Report the malaria status of this cell.
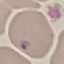
Uninfected.

Summary:
  - Preparation: thin blood film
  - Capture: smartphone through the microscope eyepiece
  - Image type: cell patch, automatically extracted from a larger field of view and resized to 64 × 64 pixels
  - Stain: Giemsa